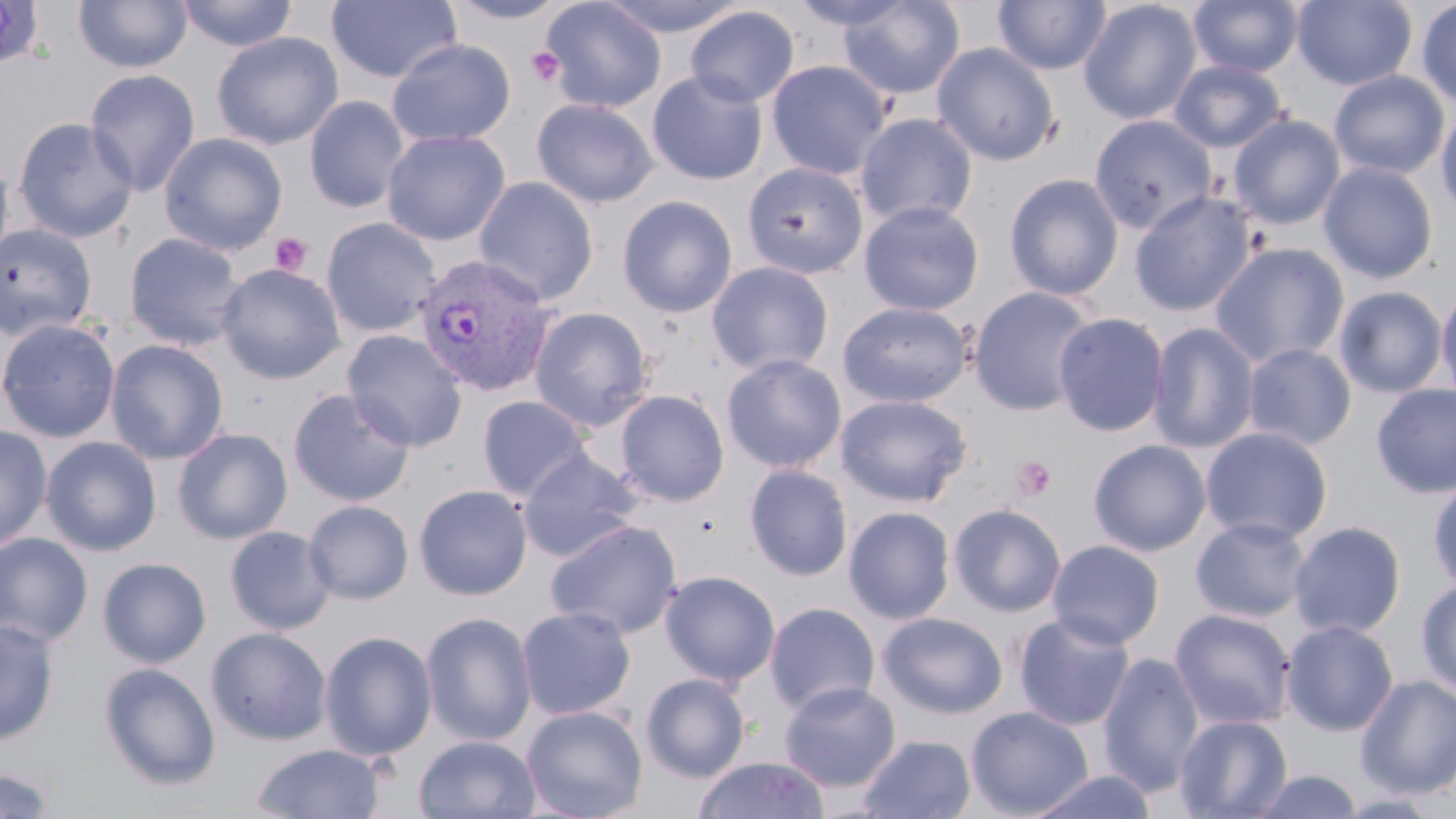
Plasmodium vivax-infected red blood cell locations = approximate bounding boxes as [x1, y1, x2, y2] in pixels: [413, 252, 560, 396]
slide-level diagnosis = Plasmodium vivax
preparation = thin blood smear
magnification = 1000x
platelet locations = approximate bounding boxes as [x1, y1, x2, y2] in pixels: [527, 46, 565, 88], [270, 233, 313, 276], [1012, 456, 1057, 500]
field of view = single
modality = optical microscopy
stain = May-Grünwald-Giemsa
uninfected red blood cell locations = approximate bounding boxes as [x1, y1, x2, y2] in pixels: [177, 0, 297, 52], [326, 0, 462, 85], [444, 0, 575, 25], [539, 0, 667, 113], [598, 0, 749, 37], [788, 0, 917, 32], [838, 0, 965, 100], [993, 0, 1111, 75], [1188, 0, 1303, 77], [1292, 0, 1417, 89], [0, 1, 45, 69], [74, 1, 192, 74], [1078, 1, 1202, 125], [1415, 1, 1456, 109], [684, 5, 800, 108], [211, 32, 343, 150], [387, 38, 516, 147], [931, 41, 1061, 166], [765, 60, 892, 180], [1169, 60, 1288, 152], [84, 69, 201, 196], [646, 70, 768, 186], [1329, 71, 1450, 180], [304, 96, 409, 214], [532, 98, 659, 208], [1436, 104, 1456, 217], [855, 113, 978, 229], [1089, 114, 1217, 235], [1228, 114, 1346, 230], [13, 116, 139, 244], [381, 130, 510, 246], [159, 133, 288, 255], [0, 152, 15, 275], [1318, 161, 1438, 284], [742, 162, 869, 279], [1004, 173, 1124, 301], [473, 176, 599, 305], [1129, 191, 1257, 317], [617, 195, 738, 318], [858, 200, 984, 316], [322, 217, 441, 338], [0, 223, 98, 341], [124, 233, 246, 351], [1209, 241, 1350, 370], [706, 261, 834, 377], [217, 263, 346, 384], [1436, 282, 1456, 408], [1333, 285, 1448, 398], [968, 286, 1098, 417], [837, 301, 973, 408], [529, 306, 654, 431], [1052, 312, 1170, 437], [0, 317, 120, 443], [1147, 321, 1261, 454], [342, 330, 468, 451], [105, 339, 228, 465], [1242, 343, 1356, 450], [722, 353, 847, 473], [1371, 383, 1456, 499], [287, 389, 416, 507], [614, 389, 729, 507], [835, 394, 972, 507], [476, 395, 592, 502], [0, 424, 52, 551], [1200, 426, 1333, 545], [172, 427, 293, 544], [41, 436, 162, 556], [1088, 439, 1211, 556], [518, 450, 643, 562], [744, 464, 853, 581], [1427, 476, 1456, 592], [413, 484, 533, 600], [304, 500, 414, 604], [947, 503, 1067, 617], [843, 506, 955, 624], [1190, 516, 1312, 623], [545, 519, 682, 639], [1288, 520, 1407, 639], [224, 526, 336, 635], [0, 533, 94, 648], [1047, 539, 1165, 649], [98, 557, 211, 667], [660, 570, 780, 686], [1416, 578, 1456, 699], [764, 602, 880, 716], [517, 606, 636, 719], [1169, 608, 1296, 730], [421, 611, 537, 747], [877, 612, 1009, 719], [1013, 612, 1136, 731], [0, 619, 60, 745], [1280, 619, 1399, 736], [206, 626, 331, 745], [318, 630, 437, 762], [1096, 651, 1206, 797], [98, 662, 221, 790], [640, 673, 751, 782], [1355, 675, 1456, 798], [779, 681, 901, 792], [521, 705, 648, 819], [966, 706, 1094, 818], [1174, 714, 1293, 819], [414, 734, 541, 818], [856, 734, 976, 819], [252, 743, 385, 819], [693, 756, 829, 818], [0, 765, 58, 818], [1026, 769, 1159, 819], [1249, 769, 1366, 818]
image size = 1456×819 pixels